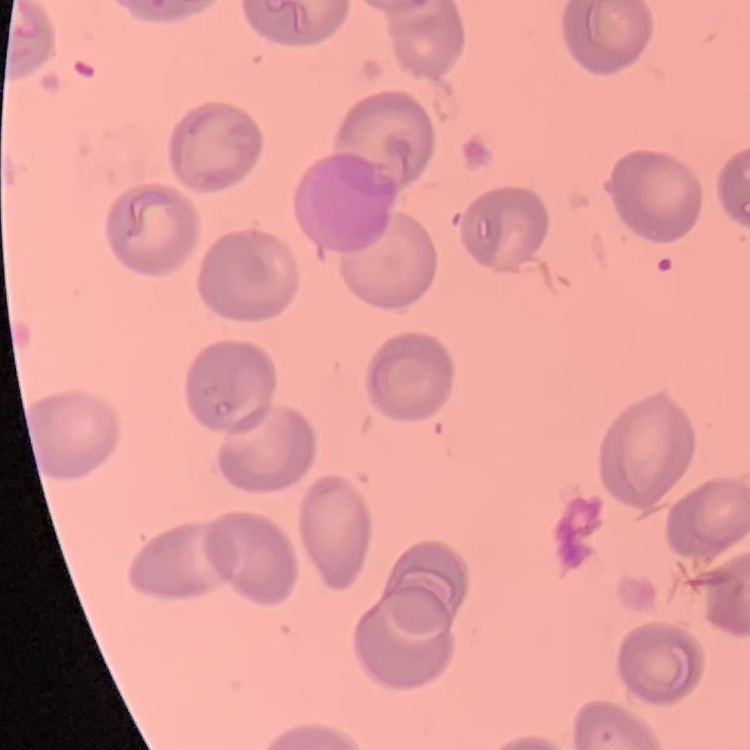

The red blood cells show no rouleaux formation. Thin blood film. Stained with either Field's or Giemsa. Square crop of a larger photomicrograph.